Assess this cell for malaria.
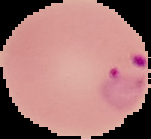

Parasitized.

Image is 151×139 pixels. The area outside the segmented cell region is set to black. From a thin blood smear.